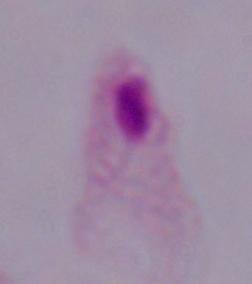
Summary:
  - Magnification: 1000x
  - Identification: trichomonad
  - Modality: photomicrograph